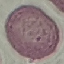
Summary:
  - Malaria status: uninfected
  - Preparation: thin blood film
  - Stain: Giemsa
  - Image type: automatically extracted cell patch, resized to 64 × 64 pixels
  - Capture: smartphone through the microscope eyepiece